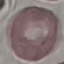
Result: negative for malaria parasites. Thin blood smear. Acquired by smartphone through the microscope eyepiece. Giemsa stain. Automatically extracted cell patch, resized to 64 × 64 pixels.